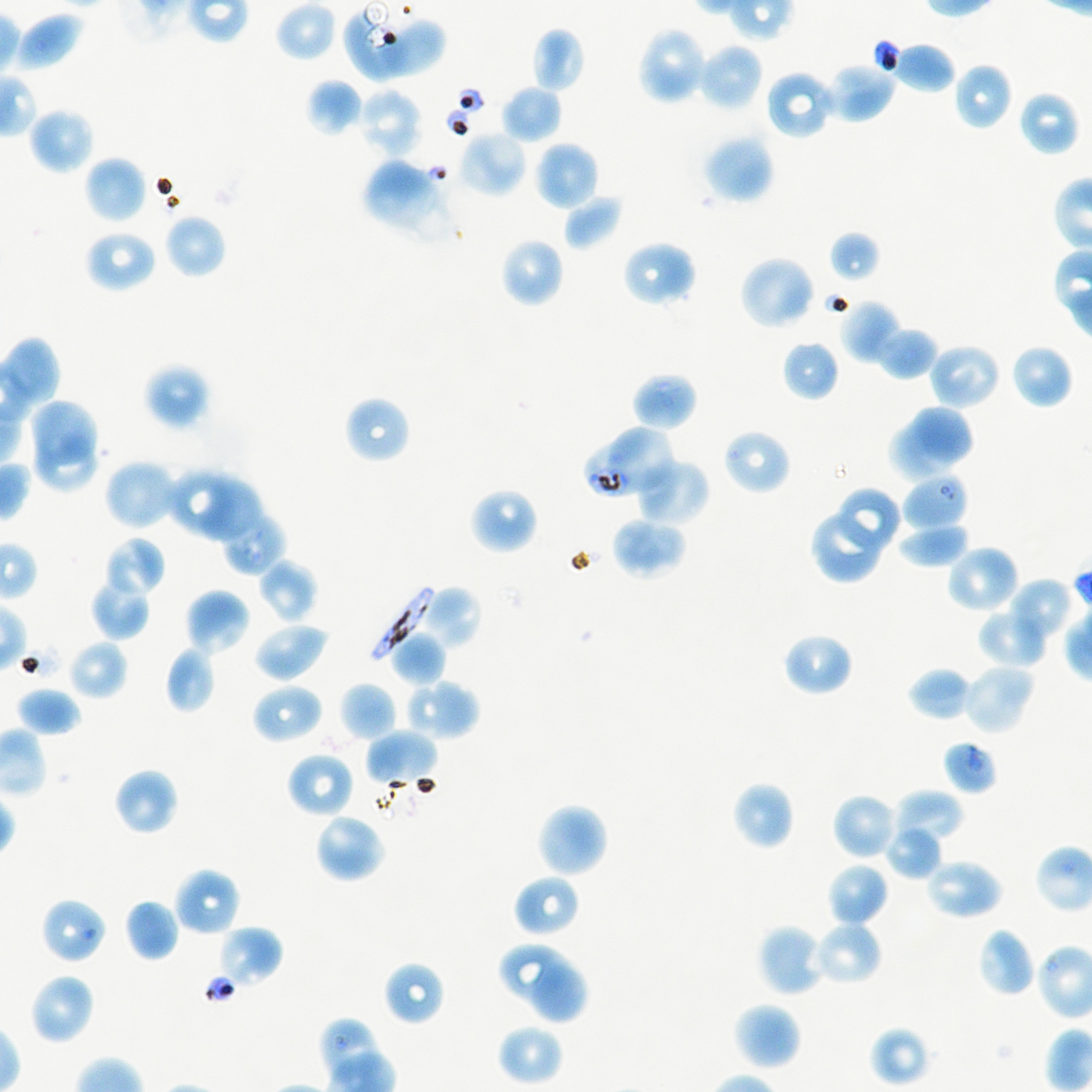
Approximate bounding boxes as {x1, y1, x2, y2} in pixels. Not every red blood cell is marked.
Summary:
  - Locations of infected red blood cells: {370, 585, 433, 660}
  - Locations of uninfected red blood cells: {274, 0, 337, 63}, {11, 10, 86, 73}, {382, 19, 447, 75}, {531, 26, 585, 93}, {640, 28, 703, 105}, {882, 39, 957, 94}, {697, 42, 764, 111}, {824, 60, 897, 123}, {953, 63, 1013, 130}, {765, 70, 836, 140}, {306, 78, 363, 137}, {501, 85, 563, 143}, {357, 87, 422, 159}, {1018, 91, 1079, 157}, {28, 107, 95, 175}, {457, 129, 528, 198}, {702, 133, 775, 204}, {534, 141, 598, 211}, {84, 156, 147, 224}, {365, 158, 439, 230}, {562, 194, 623, 250}, {164, 213, 226, 279}, {84, 230, 157, 293}, {829, 230, 881, 284}, {500, 238, 565, 308}, {621, 240, 696, 308}, {739, 255, 817, 330}, {839, 299, 901, 365}, {875, 330, 934, 380}, {781, 340, 839, 401}, {1010, 344, 1074, 410}, {930, 346, 998, 405}, {143, 363, 211, 430}, {632, 372, 698, 431}, {350, 401, 407, 459}, {31, 403, 98, 463}, {611, 403, 693, 484}, {916, 403, 972, 463}, {890, 418, 954, 483}, {722, 428, 792, 495}, {36, 441, 96, 491}, {103, 458, 183, 532}, {637, 460, 710, 526}, {165, 466, 231, 535}, {202, 479, 260, 543}, {469, 487, 539, 554}, {837, 488, 898, 551}, {219, 509, 287, 575}, {809, 514, 879, 584}, {611, 516, 687, 580}, {898, 524, 971, 569}, {105, 535, 166, 598}, {945, 544, 1020, 615}, {93, 547, 161, 628}, {257, 560, 317, 624}, {90, 577, 151, 640}, {1009, 579, 1069, 636}, {420, 585, 481, 651}, {184, 589, 250, 655}, {978, 615, 1045, 666}, {253, 621, 329, 682}, {389, 631, 448, 687}, {782, 632, 854, 697}, {67, 640, 128, 700}, {164, 646, 217, 714}, {962, 662, 1036, 735}, {907, 666, 974, 722}, {403, 678, 480, 741}, {251, 682, 323, 745}, {339, 682, 397, 742}, {16, 687, 81, 737}, {364, 729, 439, 787}, {285, 750, 355, 818}, {113, 768, 179, 836}, {731, 781, 794, 850}, {892, 789, 964, 843}, {832, 793, 898, 860}, {536, 802, 609, 878}, {313, 812, 386, 884}, {887, 828, 941, 880}, {826, 862, 890, 928}, {931, 864, 998, 915}, {172, 867, 241, 937}, {513, 873, 581, 939}, {124, 898, 180, 962}, {812, 920, 884, 986}, {757, 924, 826, 998}, {216, 926, 283, 989}, {978, 928, 1035, 998}, {499, 943, 569, 1001}, {383, 961, 445, 1025}, {531, 963, 587, 1022}, {36, 975, 90, 1040}, {732, 1002, 802, 1071}, {496, 1023, 563, 1087}, {868, 1025, 931, 1087}
  - Locations of red blood cells of indeterminate infection status: {342, 12, 405, 84}, {606, 425, 674, 490}, {583, 443, 645, 500}, {902, 475, 969, 530}, {946, 744, 993, 790}, {44, 900, 105, 962}
  - Donor blood group: A+/O+
  - Image size: 1092×1092 pixels
  - Objective: 100x, oil immersion, numerical aperture 1.45
  - Preparation: thin blood film
  - Culture: in-vitro P. falciparum strain NF54, static
  - Field of view: single
  - Stain: Giemsa